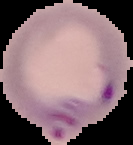 Segmented cell region on a black background. Image is 133×145 pixels. Result: Plasmodium parasites identified. From a thin blood film.